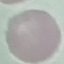
malaria status = uninfected
image type = cell patch, automatically extracted from a larger field of view and resized to 64 × 64 pixels
capture = smartphone camera at the microscope eyepiece
preparation = thin blood film
stain = Giemsa